Locate every uninfected red blood cell.
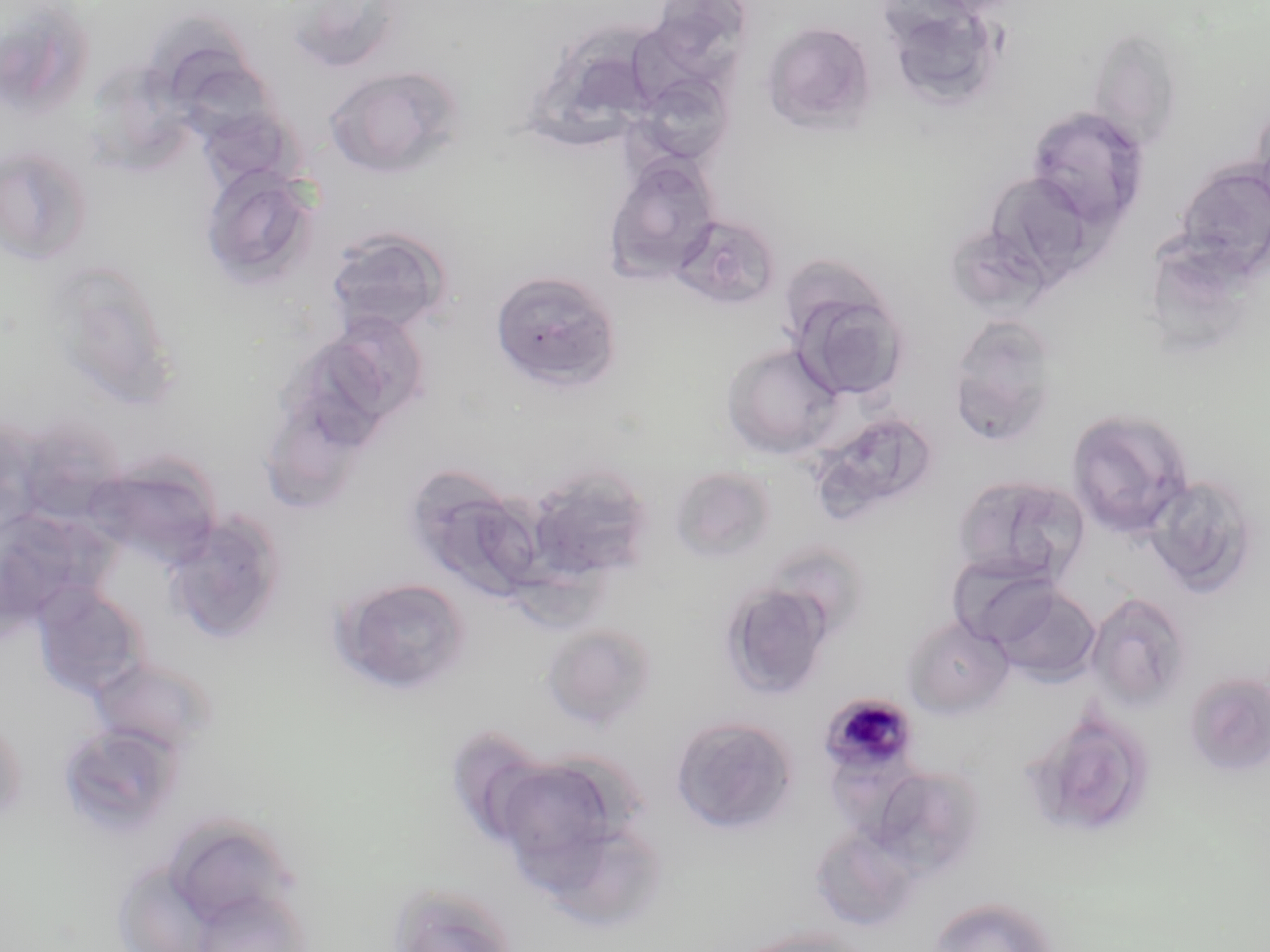
Approximate bounding boxes as (x1,y1)-(x2,y2) corner pairs in pixels.
Uninfected red blood cells: (0,3)-(96,120), (902,15)-(1024,109), (633,17)-(739,120), (142,18)-(262,134), (761,21)-(877,134), (1086,27)-(1185,152), (324,65)-(463,180), (96,68)-(197,173), (632,73)-(735,167), (1249,99)-(1270,214), (1025,106)-(1150,230), (206,112)-(317,204), (1,144)-(94,268), (603,154)-(721,284), (1174,161)-(1270,281), (200,165)-(321,291), (985,171)-(1101,284), (668,213)-(782,310), (324,226)-(454,337), (54,267)-(185,411), (489,269)-(622,392), (783,269)-(908,400), (946,315)-(1061,445), (323,316)-(428,433), (721,342)-(846,459), (271,407)-(372,511), (1067,407)-(1194,538), (0,417)-(44,542), (818,421)-(938,519), (85,448)-(234,579), (668,465)-(777,564), (404,469)-(546,604), (534,473)-(655,577), (951,474)-(1089,586), (1144,475)-(1260,596), (173,517)-(286,639), (759,540)-(870,645), (947,553)-(1064,648), (329,576)-(473,698), (720,582)-(835,701), (984,582)-(1102,685), (31,586)-(149,701), (1085,591)-(1193,712), (902,616)-(1013,718), (542,624)-(658,729), (88,655)-(217,757), (1183,672)-(1270,778), (0,713)-(28,827), (671,715)-(799,835), (56,722)-(184,837), (1044,722)-(1147,841), (866,765)-(986,880), (501,774)-(624,891), (176,821)-(297,934), (809,825)-(922,933), (387,884)-(519,952), (926,896)-(1059,952), (734,926)-(873,952).

Summary:
  - Plasmodium malariae-infected red blood cell locations: (818,692)-(921,779)
  - Slide-level diagnosis: Plasmodium malariae
  - Modality: optical microscopy
  - Stain: May-Grünwald-Giemsa
  - Preparation: thin blood film
  - Image size: 1270×952 pixels
  - Field of view: single
  - Magnification: 1000x